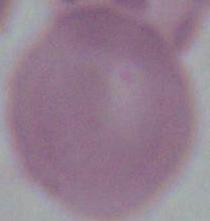

identification = red blood cell
modality = micrograph
magnification = 1000x